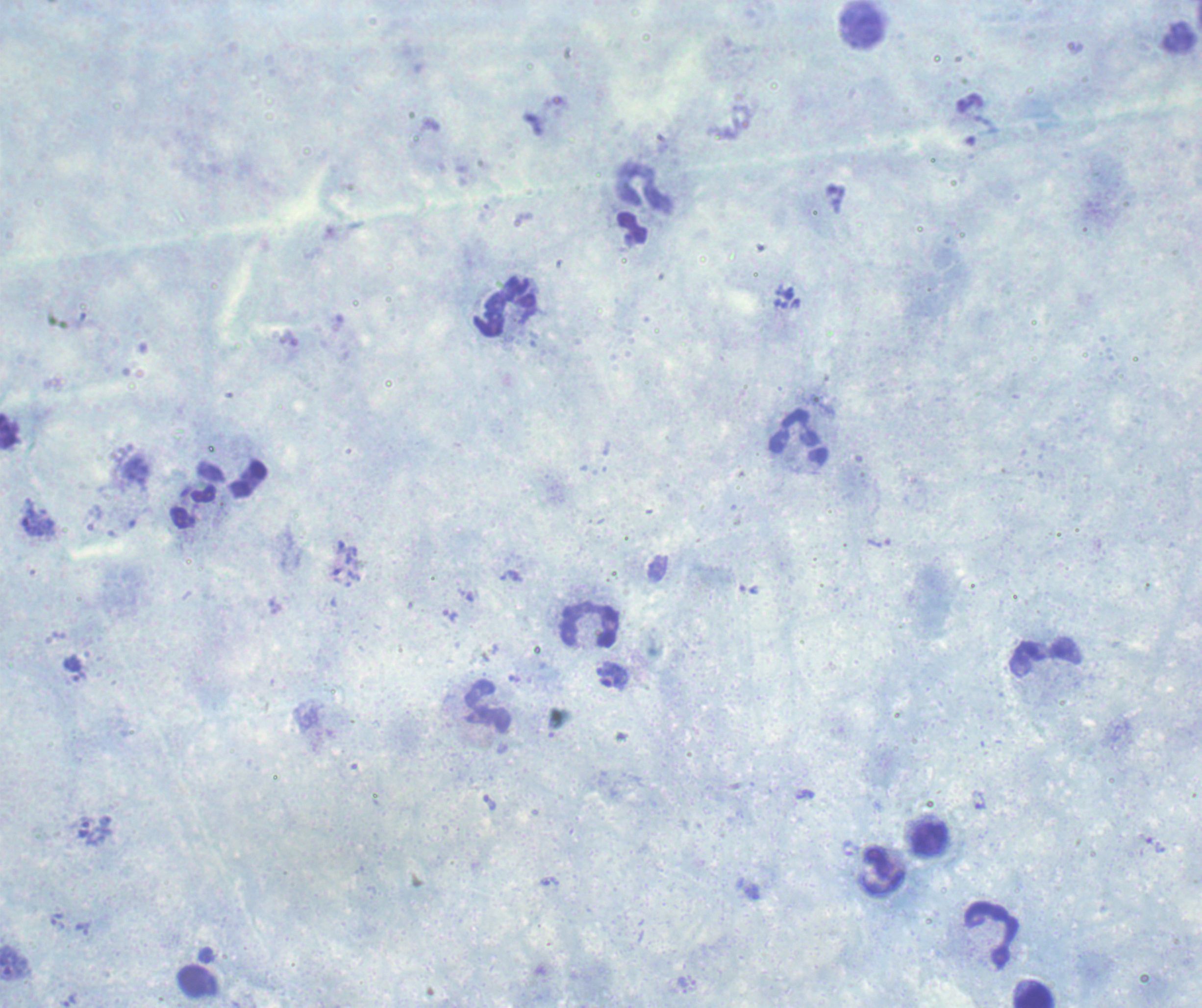

Romanowsky stain. Image is 1202×1008 pixels. Thick blood smear. Single field of view.